Give the extent of all Plasmodium falciparum-infected red blood cells.
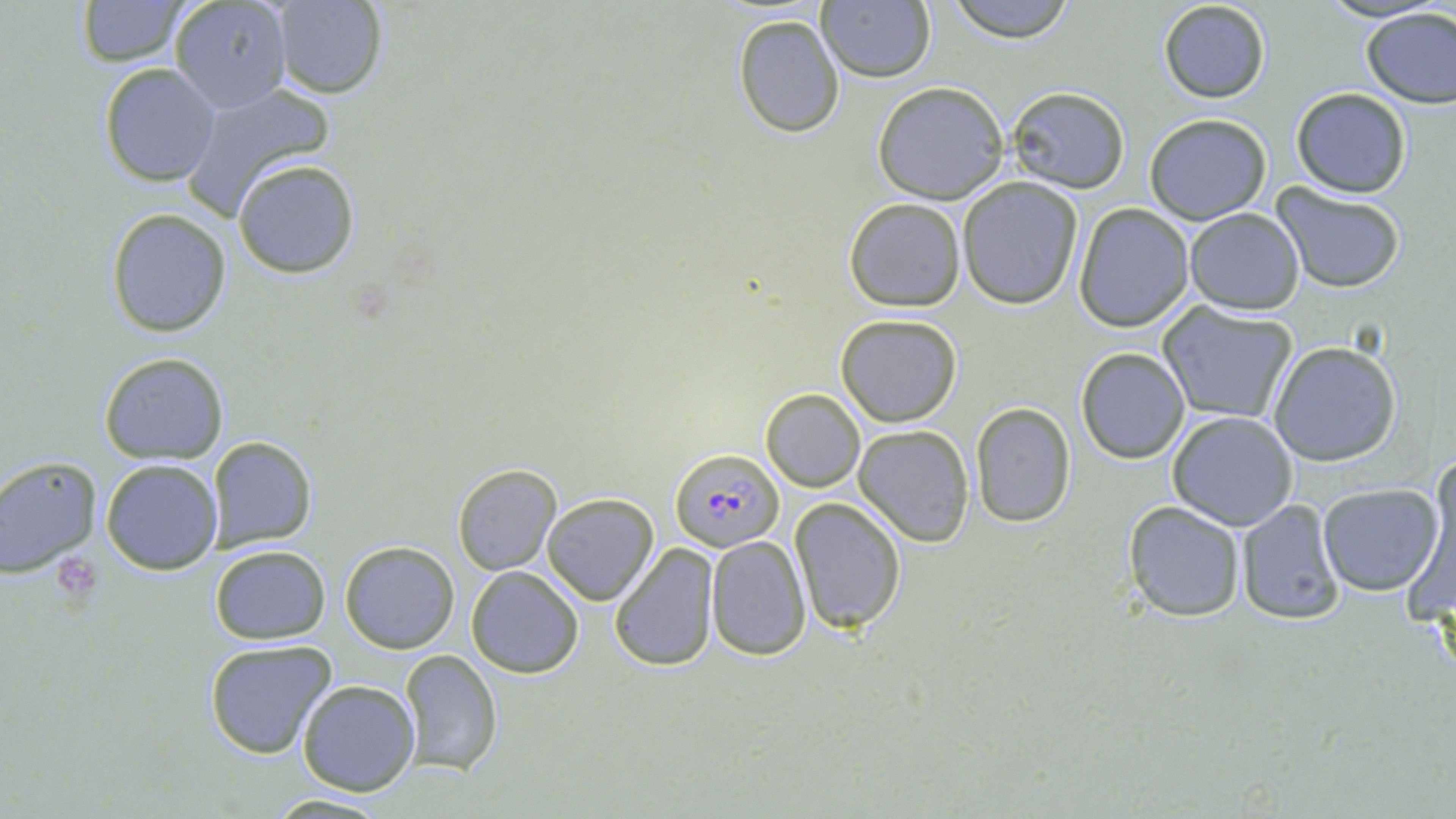
Approximate bounding boxes as (x1,y1)-(x2,y2) corner pairs in pixels.
Plasmodium falciparum-infected red blood cells: (668,446)-(785,553).

Summary:
  - Platelet locations: (56,554)-(102,599)
  - Uninfected red blood cell locations: (73,0)-(191,66), (168,0)-(292,114), (944,0)-(1078,42), (1155,0)-(1272,105), (273,1)-(387,99), (816,1)-(935,83), (1359,6)-(1456,109), (731,13)-(843,138), (97,62)-(222,186), (179,79)-(336,217), (872,81)-(1010,204), (1005,86)-(1130,194), (1291,87)-(1412,198), (1142,113)-(1272,224), (233,159)-(359,278), (956,177)-(1084,310), (1272,184)-(1407,293), (842,198)-(966,313), (1074,204)-(1196,332), (107,207)-(232,337), (1184,207)-(1305,313), (1157,303)-(1300,426), (834,314)-(962,427), (1267,340)-(1402,467), (1075,346)-(1191,463), (98,352)-(229,464), (761,389)-(865,492), (969,401)-(1077,528), (1166,411)-(1299,531), (854,424)-(975,547), (207,436)-(317,551), (1429,450)-(1455,578), (0,457)-(102,577), (100,458)-(223,575), (451,463)-(562,576), (1316,483)-(1444,595), (541,493)-(659,605), (790,497)-(907,635), (1234,500)-(1346,625), (1122,501)-(1247,622), (705,534)-(811,661), (339,541)-(460,654), (608,542)-(720,669), (210,545)-(331,645), (465,566)-(584,678), (203,637)-(339,758), (398,650)-(501,777), (296,679)-(420,797), (266,793)-(392,817)
  - Slide-level diagnosis: Plasmodium falciparum
  - Field of view: one of a larger specimen
  - Magnification: 1000x
  - Modality: light microscopy
  - Stain: May-Grünwald-Giemsa
  - Image size: 1456×819 pixels
  - Preparation: thin blood smear